State which parasite is depicted.
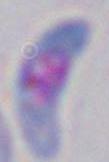

This is Toxoplasma gondii.

Summary:
  - Magnification: 1000x
  - Modality: photomicrograph